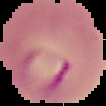
The area outside the segmented cell region is set to black. From a thin blood film. Image is 106×106 pixels. Result: malaria parasites detected.